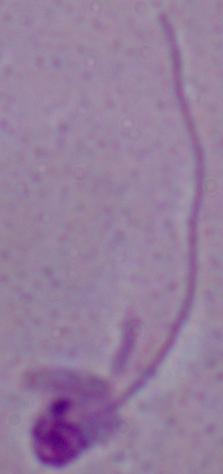

{
  "modality": "micrograph",
  "magnification": "1000x",
  "identification": "Leishmania"
}